Give the extent of all uninfected red blood cells.
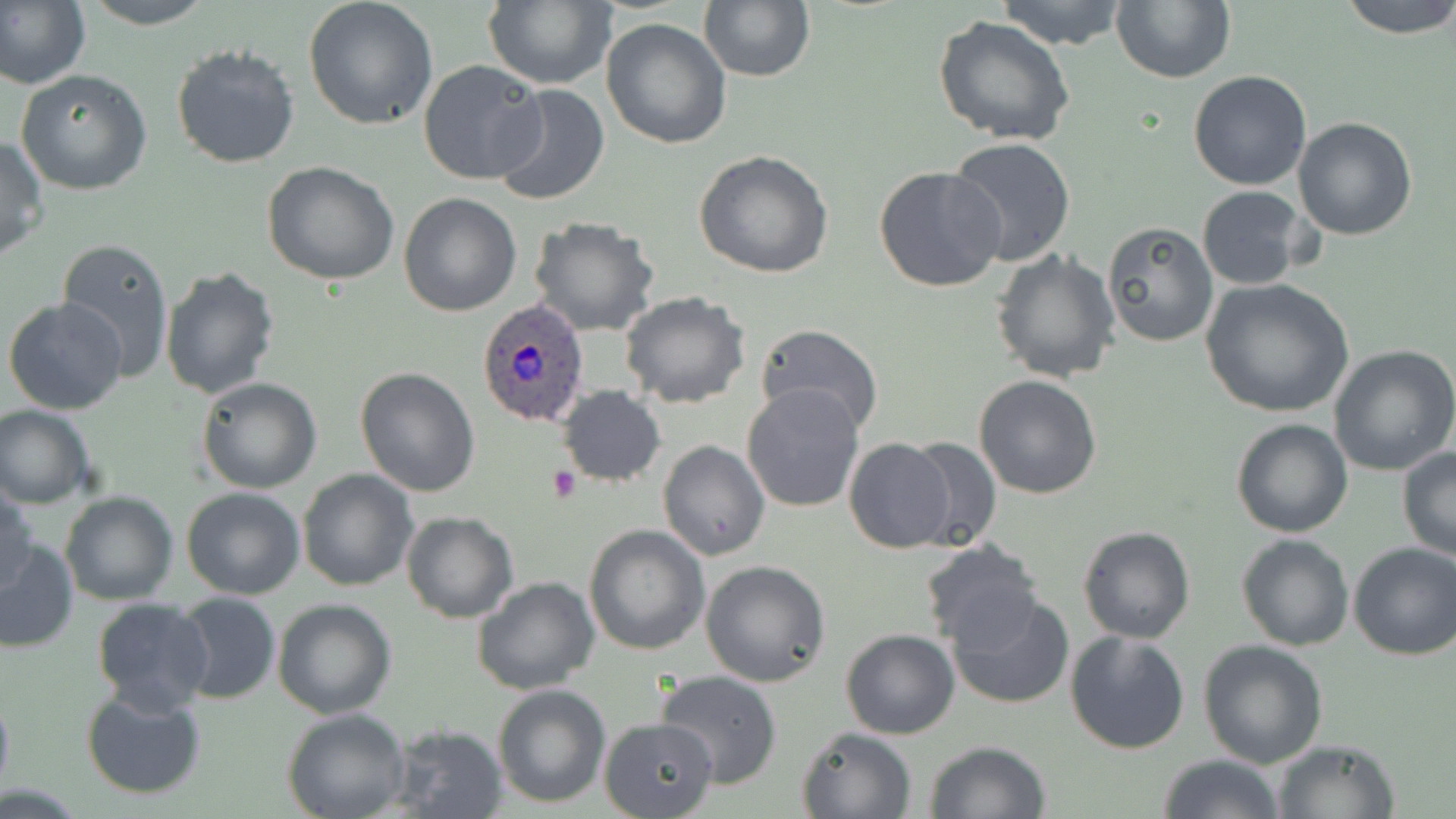

Approximate bounding boxes as (x1, y1, x2, y2) in pixels.
Uninfected red blood cells: (0, 0, 91, 93), (78, 0, 218, 28), (484, 0, 618, 90), (699, 0, 814, 82), (994, 0, 1130, 50), (1112, 0, 1236, 84), (1340, 0, 1456, 39), (304, 1, 439, 130), (932, 15, 1076, 147), (600, 18, 732, 150), (171, 43, 301, 170), (418, 59, 547, 186), (15, 69, 153, 194), (1187, 70, 1312, 191), (490, 82, 611, 208), (1292, 117, 1418, 240), (0, 135, 48, 260), (945, 138, 1077, 265), (694, 150, 836, 279), (263, 161, 401, 285), (873, 165, 1006, 295), (1196, 185, 1311, 290), (399, 191, 522, 316), (529, 216, 660, 336), (1100, 221, 1219, 348), (56, 237, 175, 380), (990, 248, 1120, 383), (159, 263, 281, 398), (1200, 278, 1355, 418), (618, 292, 751, 408), (3, 298, 129, 417), (755, 322, 884, 433), (1328, 345, 1456, 476), (354, 367, 480, 498), (974, 373, 1104, 499), (197, 377, 322, 494), (742, 383, 864, 513), (557, 385, 666, 487), (0, 404, 95, 509), (1230, 418, 1354, 538), (903, 435, 1004, 551), (844, 438, 957, 553), (657, 440, 770, 561), (1396, 447, 1456, 562), (297, 469, 418, 591), (1, 480, 37, 595), (181, 486, 306, 600), (60, 490, 177, 605), (400, 510, 519, 623), (583, 524, 710, 655), (1077, 525, 1197, 643), (1236, 533, 1354, 651), (0, 538, 77, 654), (918, 541, 1046, 653), (1347, 542, 1455, 660), (700, 561, 831, 687), (471, 577, 601, 696), (946, 588, 1076, 710), (172, 593, 280, 705), (92, 597, 214, 713), (272, 598, 397, 719), (841, 628, 960, 739), (1064, 629, 1192, 755), (1197, 639, 1329, 770), (656, 669, 783, 789), (492, 683, 611, 807), (0, 686, 13, 802), (80, 688, 207, 800), (283, 709, 410, 819), (599, 716, 719, 819), (386, 724, 510, 818), (796, 727, 916, 819), (1269, 738, 1400, 818), (923, 740, 1053, 819), (1159, 753, 1285, 819).

slide-level diagnosis = Plasmodium ovale
modality = optical microscopy
image size = 1456×819 pixels
magnification = 1000x
stain = May-Grünwald-Giemsa
field of view = one of a larger specimen
preparation = thin blood film
platelet locations = approximate bounding boxes as (x1, y1, x2, y2) in pixels: (548, 464, 583, 505)
Plasmodium ovale-infected red blood cell locations = approximate bounding boxes as (x1, y1, x2, y2) in pixels: (478, 299, 590, 428)